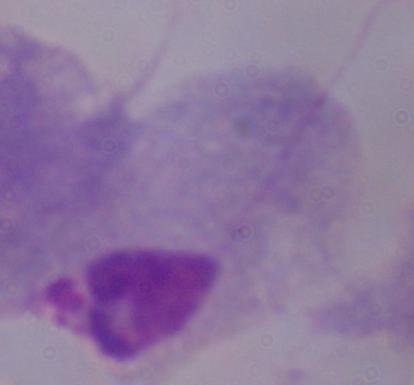
Micrograph. Captured at 1000x magnification. A trichomonad is shown.